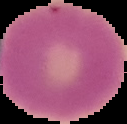

Image is 127×124 pixels. Malaria status: uninfected. From a thin blood film. Segmented cell region on a black background.